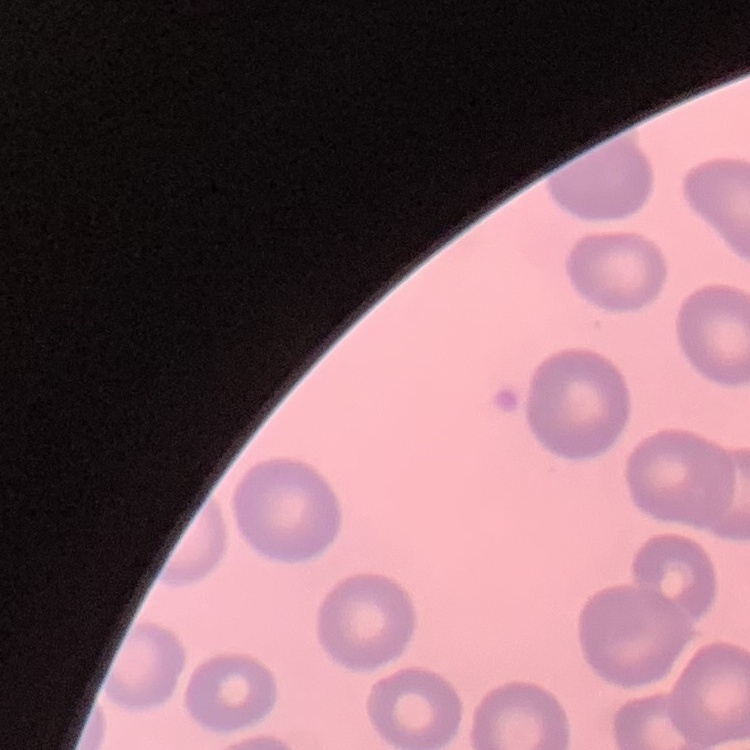
The erythrocytes exhibit no rouleaux formation. Thin blood smear. One tile cut from a larger photomicrograph. Stained with either Field's or Giemsa.